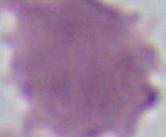

Summary:
  - Identification: erythrocyte
  - Modality: micrograph
  - Magnification: 1000x